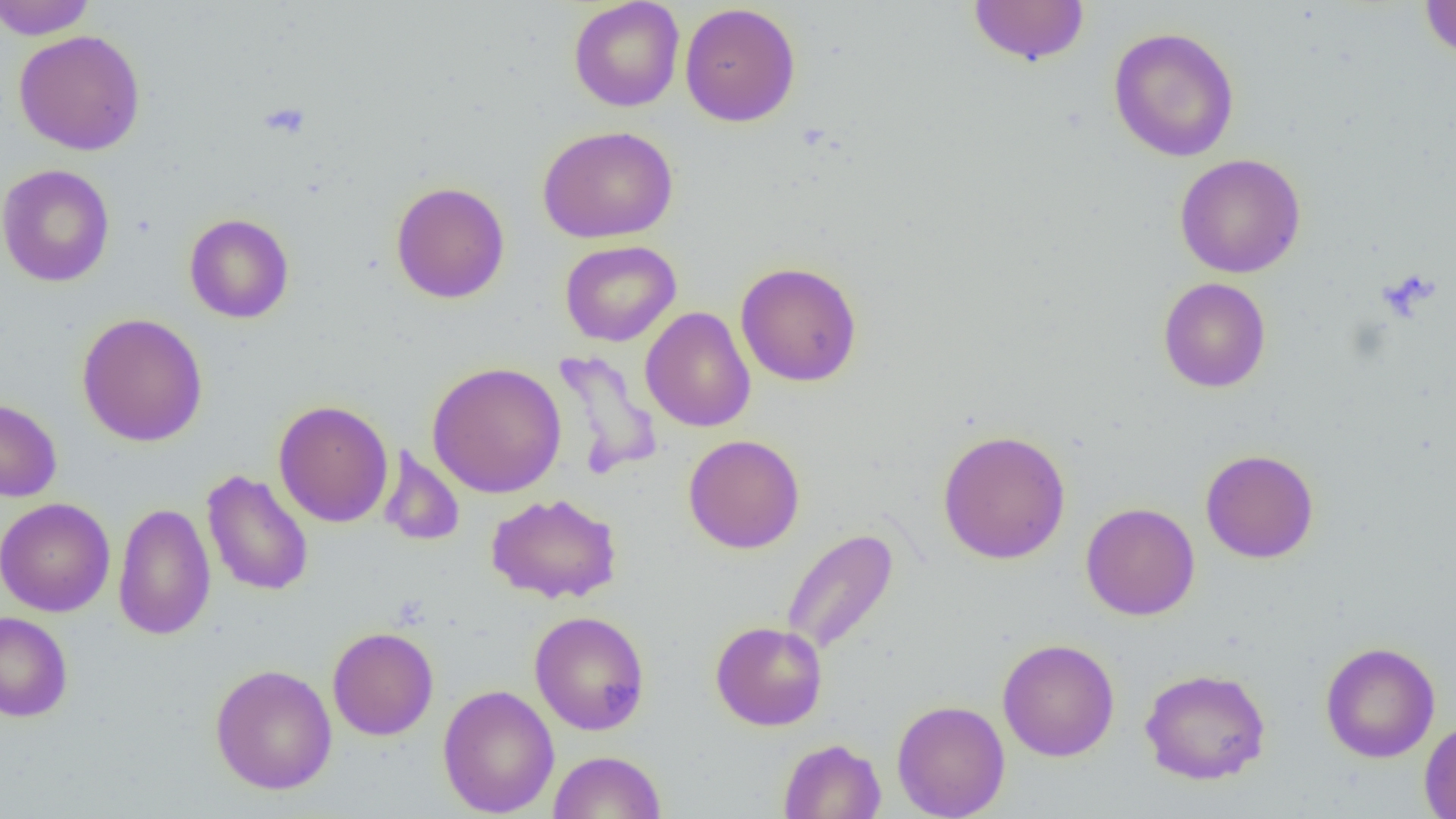

{
  "slide_level_diagnosis": "no evidence of blood parasites",
  "preparation": "thin blood smear",
  "magnification": "1000x",
  "field_of_view": "single",
  "uninfected_red_blood_cell_locations": "approximate bounding boxes as (x1, y1, x2, y2) in pixels: (0, 0, 97, 39), (568, 0, 685, 112), (967, 0, 1090, 66), (1419, 0, 1456, 60), (679, 3, 801, 127), (1108, 26, 1240, 162), (13, 29, 146, 156), (538, 125, 678, 243), (1175, 153, 1306, 278), (0, 164, 115, 287), (391, 181, 511, 304), (184, 213, 295, 324), (560, 240, 681, 347), (735, 261, 862, 387), (1158, 277, 1271, 392), (641, 307, 756, 433), (77, 312, 208, 447), (552, 351, 663, 479), (427, 361, 567, 499), (0, 398, 62, 502), (273, 399, 394, 528), (937, 429, 1071, 564), (683, 434, 805, 553), (379, 444, 465, 548), (1200, 449, 1319, 563), (202, 469, 314, 597), (486, 492, 623, 604), (0, 497, 115, 616), (113, 502, 216, 640), (1080, 502, 1200, 621), (780, 527, 899, 657), (529, 610, 650, 736), (0, 611, 73, 722), (710, 621, 827, 731), (327, 626, 439, 740), (997, 638, 1120, 762), (1320, 641, 1440, 763), (210, 663, 337, 795), (1139, 667, 1271, 784), (438, 684, 559, 817), (892, 699, 1010, 819), (1419, 720, 1456, 818), (778, 738, 886, 819), (548, 750, 667, 819)",
  "image_size": "1456×819 pixels",
  "platelet_locations": "approximate bounding boxes as (x1, y1, x2, y2) in pixels: (259, 102, 311, 141)",
  "modality": "optical microscopy"
}